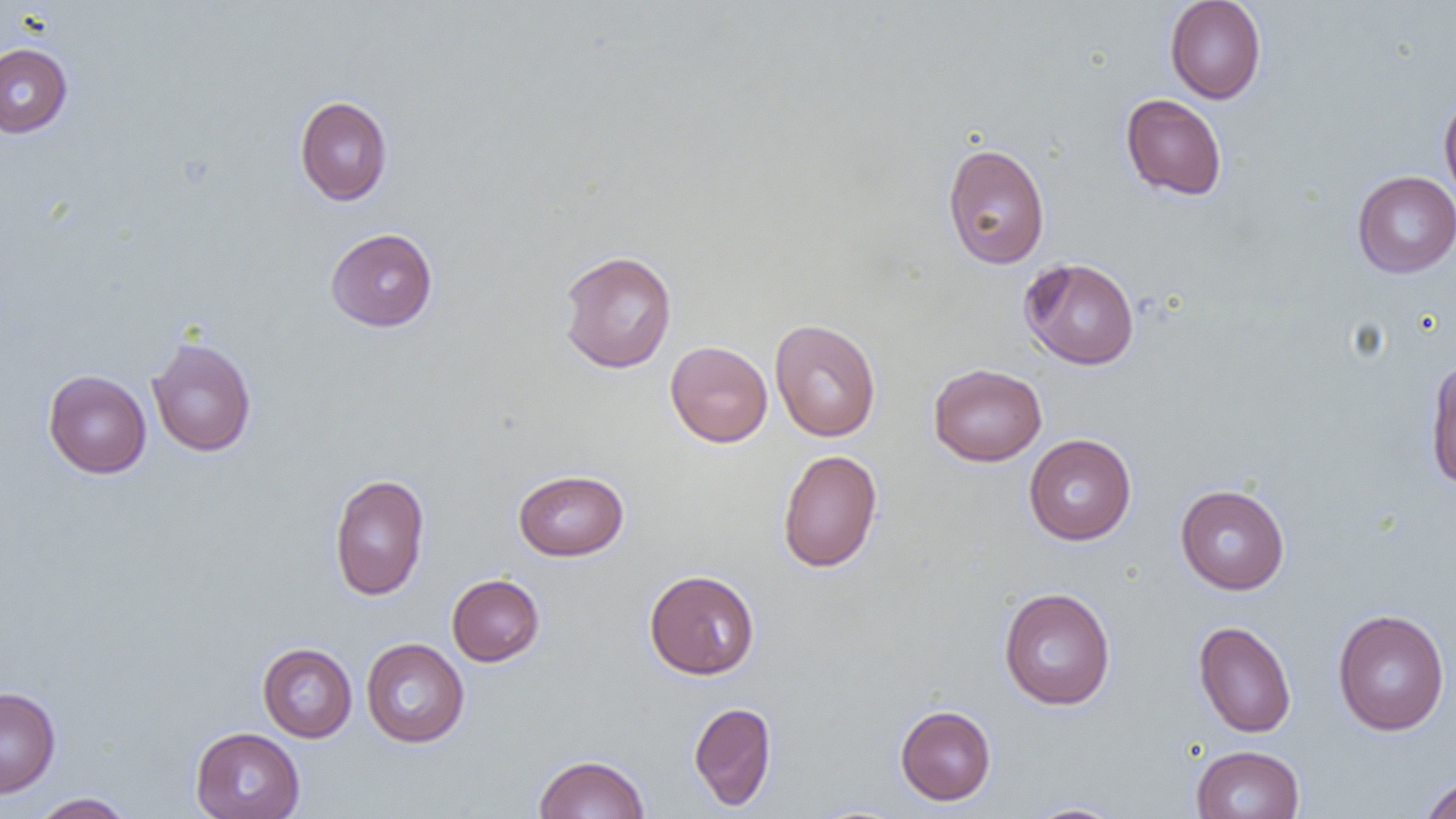

Approximate bounding boxes as named x1/y1/x2/y2 corners in pixels. Uninfected red blood cell locations: (x1=1164, y1=0, x2=1266, y2=104), (x1=0, y1=42, x2=73, y2=138), (x1=1439, y1=92, x2=1456, y2=209), (x1=1120, y1=93, x2=1228, y2=201), (x1=294, y1=95, x2=393, y2=206), (x1=942, y1=143, x2=1050, y2=269), (x1=1352, y1=171, x2=1456, y2=278), (x1=325, y1=227, x2=438, y2=331), (x1=558, y1=250, x2=677, y2=374), (x1=1019, y1=257, x2=1140, y2=370), (x1=769, y1=319, x2=881, y2=442), (x1=146, y1=336, x2=257, y2=457), (x1=665, y1=341, x2=773, y2=447), (x1=1425, y1=357, x2=1456, y2=489), (x1=928, y1=363, x2=1047, y2=466), (x1=43, y1=370, x2=152, y2=478), (x1=1023, y1=433, x2=1136, y2=545), (x1=777, y1=449, x2=882, y2=573), (x1=513, y1=469, x2=629, y2=561), (x1=328, y1=473, x2=430, y2=601), (x1=1175, y1=484, x2=1290, y2=594), (x1=644, y1=569, x2=760, y2=679), (x1=447, y1=574, x2=544, y2=666), (x1=999, y1=587, x2=1115, y2=710), (x1=1332, y1=608, x2=1450, y2=736), (x1=1193, y1=620, x2=1296, y2=738), (x1=361, y1=638, x2=469, y2=748), (x1=257, y1=642, x2=357, y2=742), (x1=0, y1=687, x2=60, y2=798), (x1=689, y1=701, x2=777, y2=810), (x1=895, y1=705, x2=996, y2=806), (x1=190, y1=727, x2=305, y2=819), (x1=1191, y1=745, x2=1305, y2=819), (x1=533, y1=754, x2=650, y2=818), (x1=1420, y1=774, x2=1456, y2=819), (x1=30, y1=792, x2=135, y2=819), (x1=1022, y1=802, x2=1129, y2=818). Slide-level diagnosis: negative for blood parasites. Captured at 1000x magnification. Thin blood smear. Image is 1456×819 pixels. One field of a larger specimen. Optical microscopy.